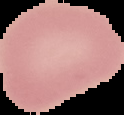

The area outside the segmented cell region is set to black. From a thin blood film. Result: no Plasmodium parasites seen. Image is 124×115 pixels.